Assess for malaria.
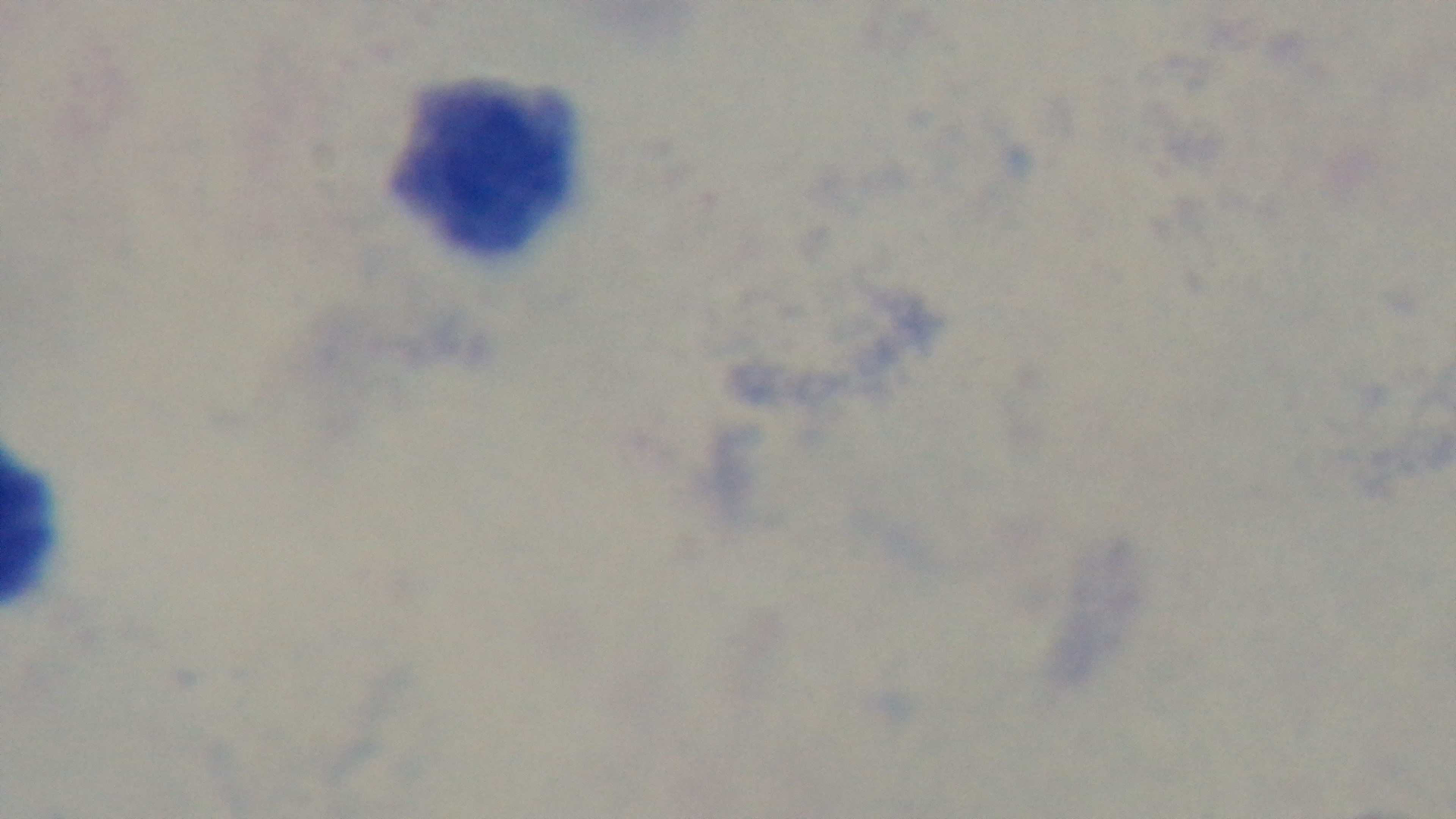

It is uninfected.

Summary:
  - Capture: mounted 4K digital camera
  - Objective: 100x oil immersion
  - Preparation: thick
  - Stain: Giemsa
  - Modality: light microscopy
  - Field of view: single